Outline each blood parasite and name the species.
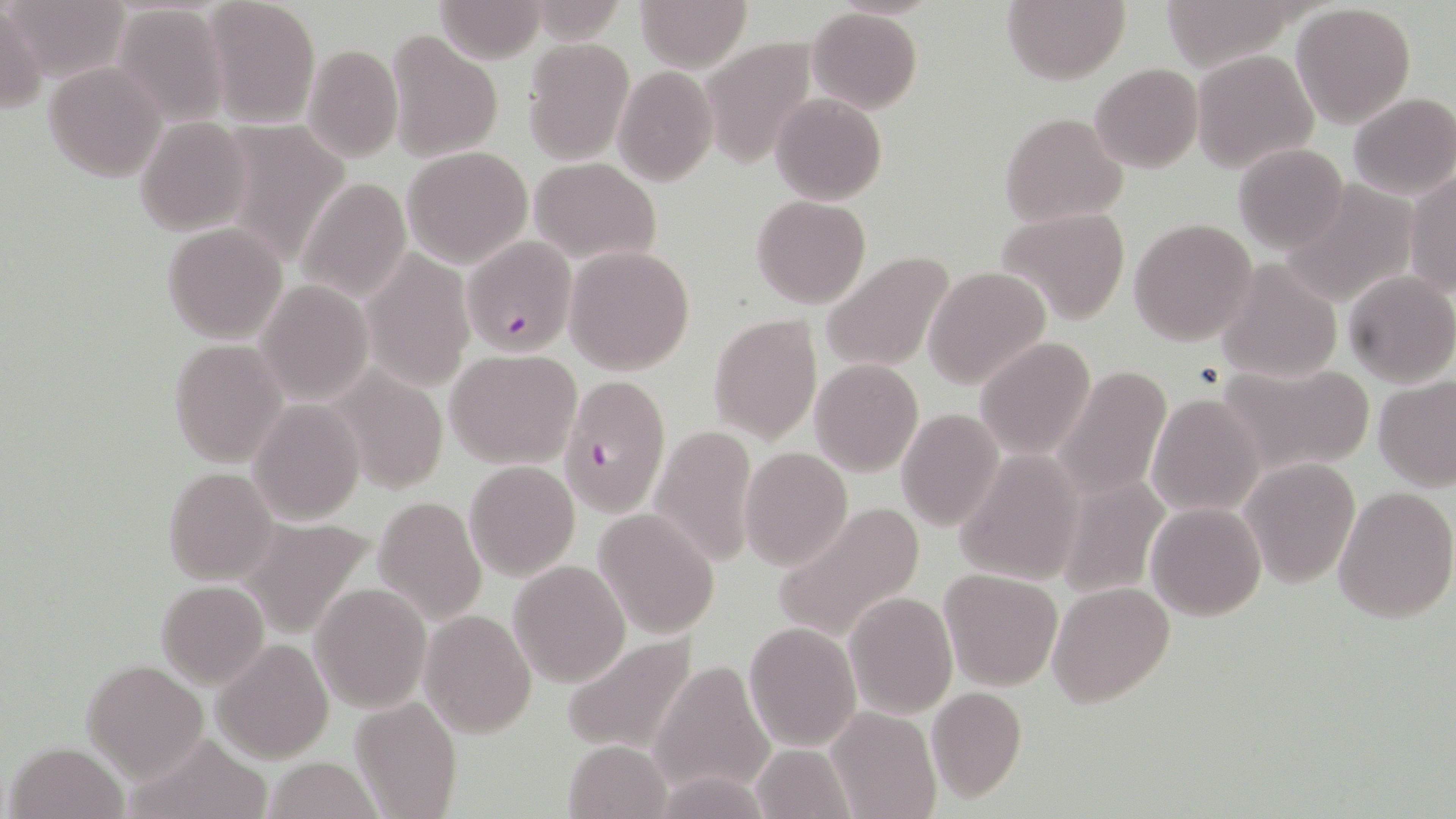
Approximate bounding boxes as [x1, y1, x2, y2] in pixels.
Plasmodium falciparum-infected red blood cells: [462, 235, 578, 357], [558, 375, 670, 516].
No Plasmodium ovale, Plasmodium malariae, Plasmodium vivax, Babesia divergens, or Trypanosoma brucei observed.

Uninfected red blood cell locations: [10, 0, 129, 82], [204, 0, 321, 127], [435, 0, 547, 62], [635, 0, 753, 70], [1001, 0, 1129, 83], [1156, 0, 1302, 69], [0, 4, 47, 114], [111, 4, 229, 126], [1291, 4, 1417, 129], [806, 7, 921, 113], [53, 14, 215, 166], [386, 29, 504, 163], [699, 36, 820, 168], [521, 38, 634, 164], [302, 43, 402, 164], [1192, 49, 1321, 174], [44, 63, 165, 181], [1090, 64, 1203, 172], [613, 67, 716, 185], [1348, 92, 1456, 200], [771, 93, 887, 204], [998, 110, 1129, 227], [135, 116, 252, 237], [203, 119, 353, 275], [1233, 143, 1350, 253], [402, 145, 533, 268], [529, 157, 660, 264], [1406, 175, 1456, 296], [297, 178, 411, 304], [1278, 179, 1421, 308], [751, 195, 871, 308], [996, 207, 1132, 325], [1128, 217, 1259, 348], [160, 223, 288, 345], [564, 244, 695, 374], [360, 250, 475, 390], [819, 250, 958, 374], [1215, 258, 1344, 383], [923, 266, 1051, 392], [1342, 272, 1456, 388], [255, 281, 373, 405], [708, 312, 822, 444], [975, 337, 1095, 460], [169, 339, 286, 466], [445, 349, 582, 468], [810, 359, 923, 476], [1055, 362, 1171, 499], [1217, 362, 1375, 477], [329, 369, 448, 494], [1374, 375, 1456, 490], [1146, 392, 1267, 518], [247, 400, 364, 526], [896, 408, 1004, 532], [649, 423, 759, 566], [739, 446, 852, 570], [953, 450, 1085, 585], [1238, 459, 1360, 589], [463, 460, 581, 581], [163, 466, 279, 585], [1057, 467, 1171, 598], [1332, 484, 1456, 624], [373, 496, 487, 625], [770, 500, 925, 642], [1145, 502, 1267, 621], [594, 510, 720, 639], [238, 514, 380, 638], [508, 560, 632, 688], [940, 568, 1063, 690], [155, 581, 269, 687], [1046, 582, 1175, 709], [310, 583, 431, 714], [845, 591, 957, 718], [419, 608, 537, 738], [743, 621, 862, 753], [559, 632, 698, 756], [212, 638, 334, 763], [82, 660, 207, 779], [651, 660, 776, 798], [926, 686, 1027, 802], [350, 696, 460, 819], [826, 705, 941, 818], [124, 731, 274, 819], [562, 739, 671, 818], [7, 741, 127, 819], [751, 744, 857, 819], [263, 757, 383, 819], [652, 771, 775, 818]. Slide-level diagnosis: Plasmodium falciparum. Thin blood film. May-Grünwald-Giemsa stain. Optical microscopy. 1000x magnification. Single field of view. Image is 1456×819 pixels.